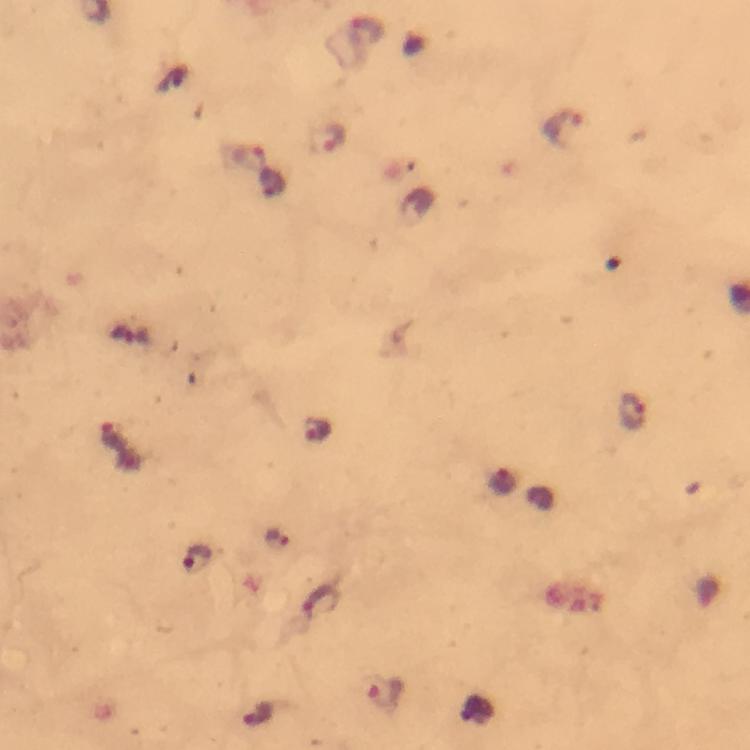

Approximate centers as [x, y] in pixels.
Summary:
  - Plasmodium parasite locations: [564, 128], [326, 139], [633, 412], [313, 429], [111, 433], [278, 540], [199, 559], [322, 602], [384, 696]
  - Stain: Giemsa
  - Image size: 750×750 pixels
  - Magnification: 100x
  - Cropped from: one field of view
  - Capture: smartphone camera through the microscope
  - Preparation: thick blood film
  - Immersion oil: applied
  - Context: from a diagnostic examination for malaria